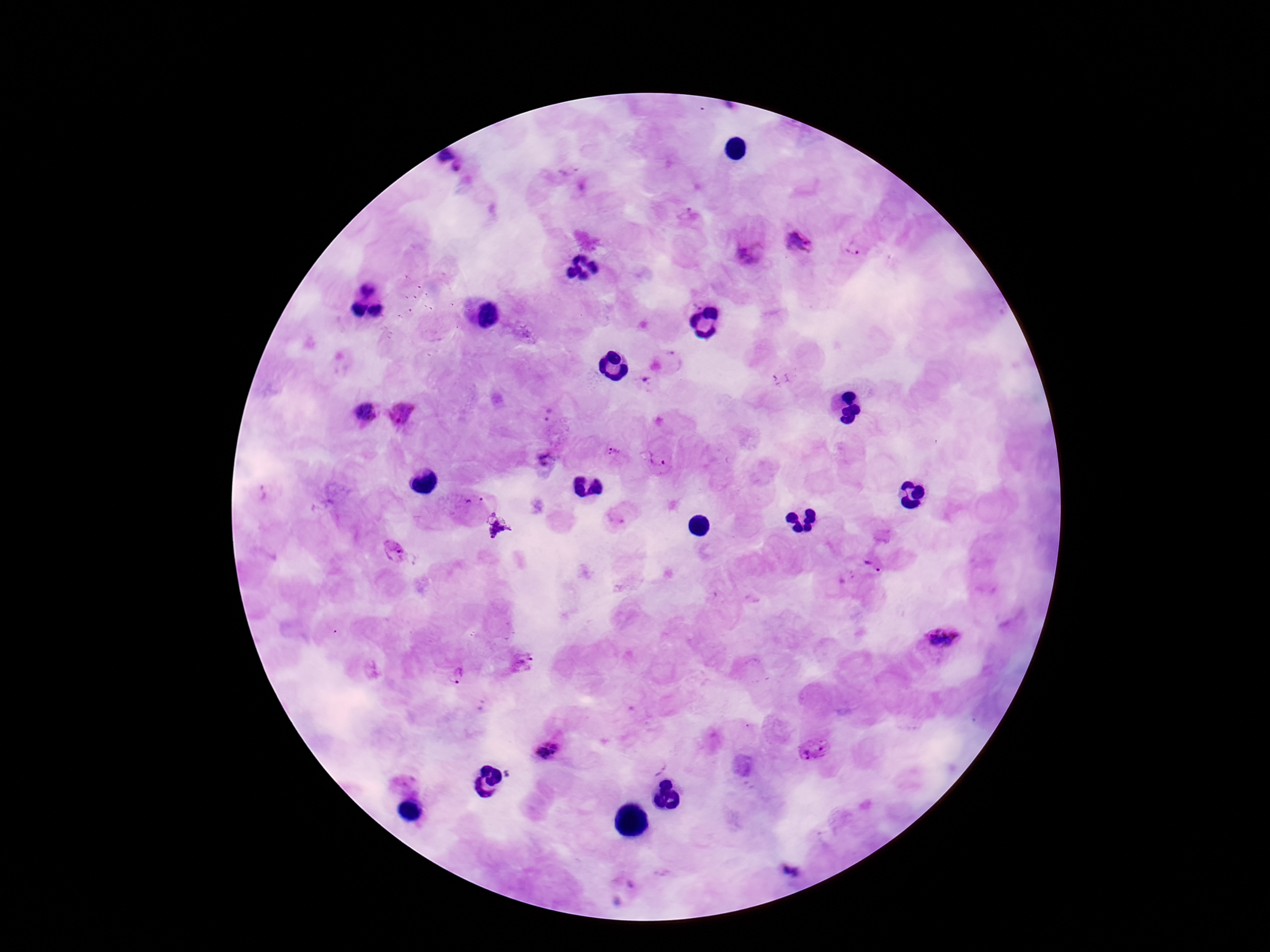
Approximate centers as (x, y) in pixels.
Summary:
  - Plasmodium parasite locations: (454, 162), (802, 241), (854, 247), (749, 250), (672, 360), (644, 382), (363, 411), (403, 414), (548, 415), (615, 456), (658, 460), (547, 461), (475, 500), (497, 530), (393, 552), (873, 565), (942, 640), (456, 674), (547, 749), (814, 751), (790, 871)
  - Field of view: one from this slide
  - Preparation: thick blood smear
  - Patient malaria status: infected
  - Stain: Giemsa
  - Magnification: 100x
  - Capture: smartphone camera through the microscope eyepiece
  - Image size: 1270×952 pixels